Name the cell type shown.
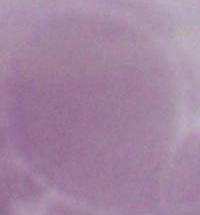

This is an erythrocyte.

Summary:
  - Magnification: 1000x
  - Modality: photomicrograph